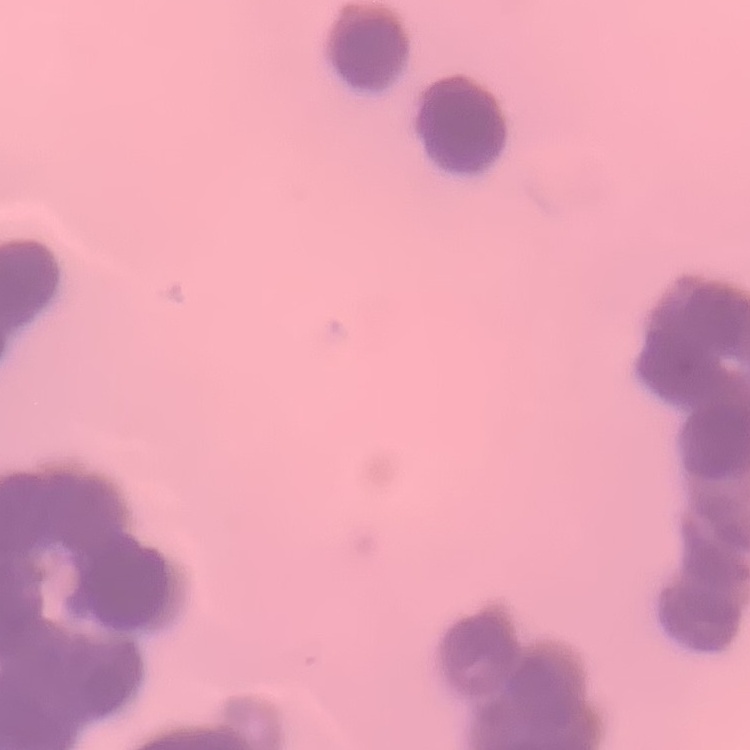

{
  "erythrocyte_morphology": "rouleaux formation",
  "preparation": "thin blood film",
  "stain": "Field's or Giemsa",
  "image_type": "square crop of a larger photomicrograph"
}